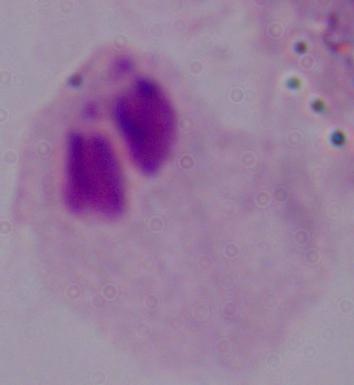

{
  "identification": "trichomonad",
  "magnification": "1000x",
  "modality": "photomicrograph"
}